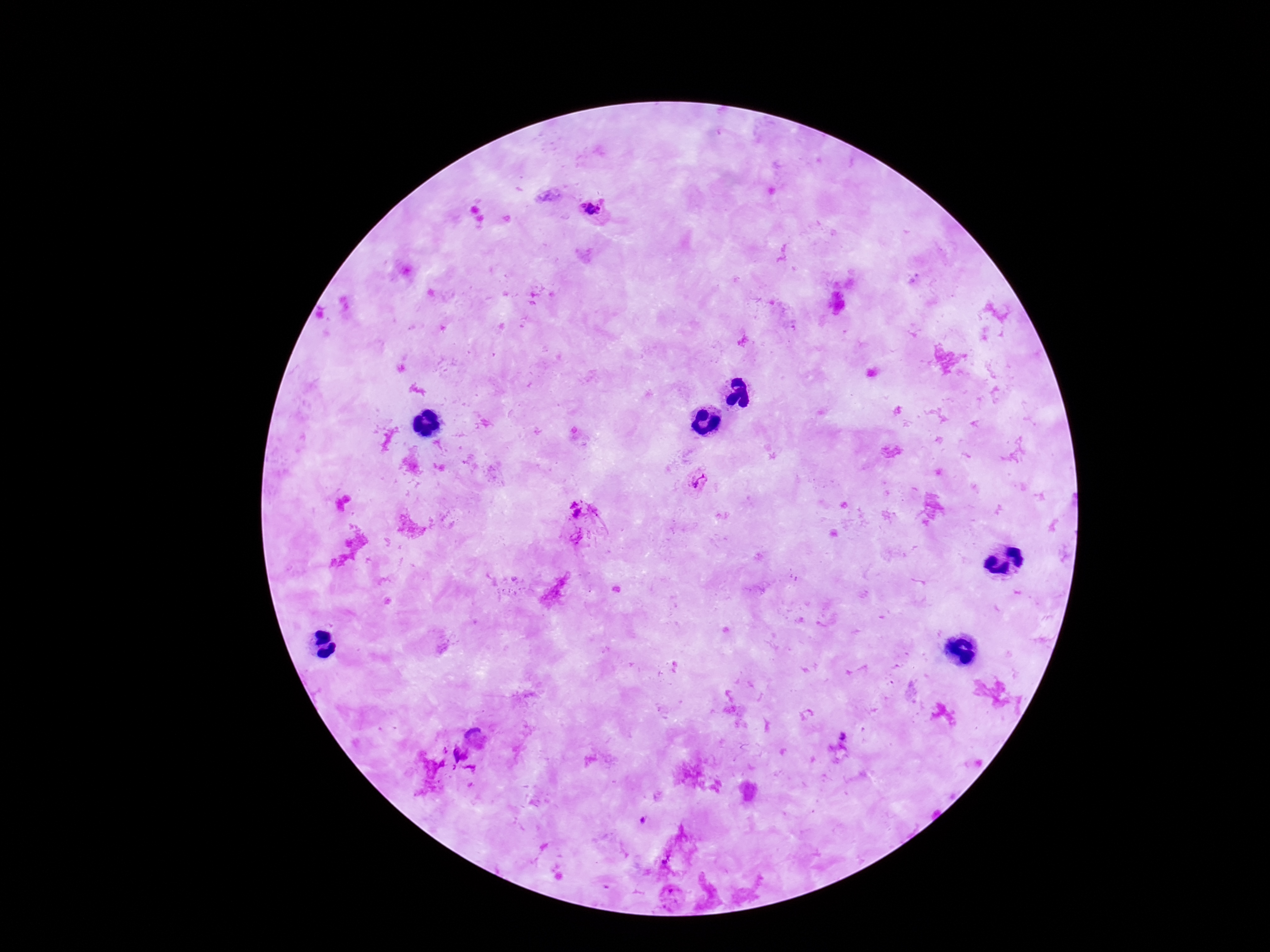
{
  "image_size": "1270×952 pixels",
  "magnification": "100x",
  "patient_malaria_status": "infected",
  "plasmodium_parasite_locations": "approximate centers as [x, y] in pixels: [589, 209], [698, 481], [575, 509], [475, 737], [460, 755], [666, 858], [670, 892]",
  "capture": "smartphone camera through the microscope eyepiece",
  "field_of_view": "one from this slide",
  "preparation": "thick peripheral-blood smear",
  "stain": "Giemsa"
}